Classify this cell by malaria status.
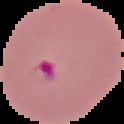

Parasitized.

From a thin blood smear. Cell region segmented out of the field of view; the surrounding area is masked to black. Image is 124×124 pixels.